Assess this cell for malaria.
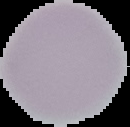
Uninfected.

From a thin blood film. Image is 130×127 pixels. Cell region segmented out of the field of view; the surrounding area is masked to black.